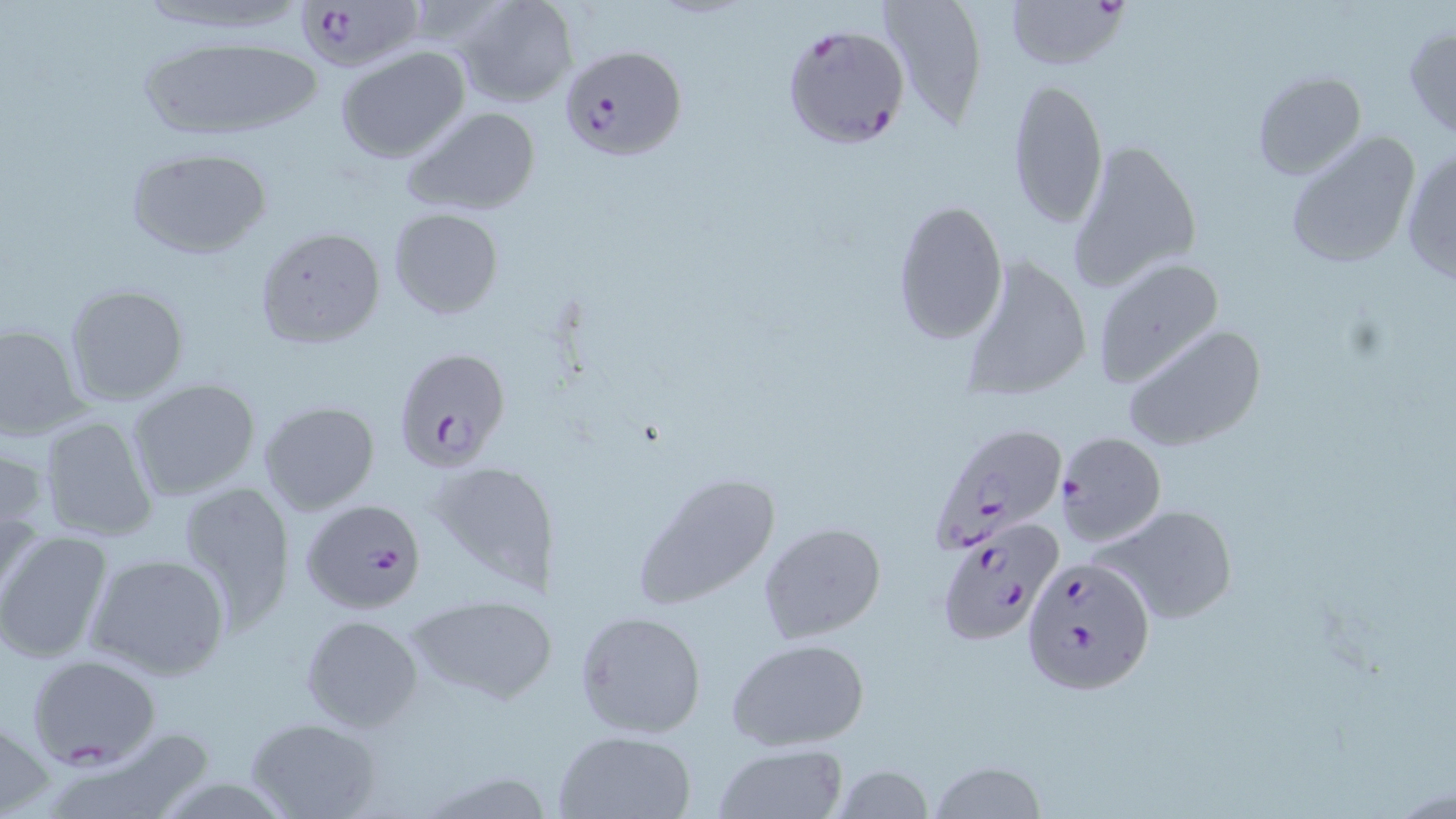 Approximate bounding boxes as (x1,y1)-(x2,y2) corner pairs in pixels. Uninfected red blood cell locations: (128,0)-(323,38), (452,0)-(578,107), (877,0)-(990,127), (1404,23)-(1456,139), (130,35)-(325,146), (336,45)-(471,164), (1250,70)-(1368,181), (1006,76)-(1108,229), (400,105)-(543,216), (1283,130)-(1423,270), (1064,136)-(1204,295), (122,144)-(274,259), (1400,145)-(1456,287), (891,198)-(1009,344), (388,208)-(504,319), (253,225)-(386,349), (958,253)-(1092,402), (1090,257)-(1225,388), (63,283)-(191,406), (0,321)-(89,440), (1121,324)-(1265,453), (125,378)-(263,503), (258,399)-(379,515), (36,414)-(160,543), (0,444)-(51,578), (426,459)-(557,594), (633,469)-(785,608), (174,481)-(296,632), (1096,502)-(1239,626), (758,521)-(887,646), (0,527)-(115,665), (85,552)-(232,681), (407,593)-(556,704), (574,610)-(707,738), (299,614)-(424,732), (726,639)-(870,751), (0,710)-(52,818), (244,717)-(381,819), (553,729)-(696,818), (44,731)-(217,819), (712,745)-(847,819), (928,761)-(1047,819), (829,763)-(935,819). Plasmodium falciparum-infected red blood cell locations: (290,0)-(428,74), (1006,0)-(1130,72), (780,23)-(913,150), (560,45)-(688,160), (393,347)-(510,471), (929,421)-(1071,552), (1056,431)-(1167,545), (300,497)-(428,614), (933,525)-(1111,656), (1021,554)-(1154,695), (26,653)-(162,769). Slide-level diagnosis: Plasmodium falciparum. Thin blood film. Single field of view. Image is 1456×819 pixels. Optical microscopy. May-Grünwald-Giemsa-stained preparation. 1000x magnification.